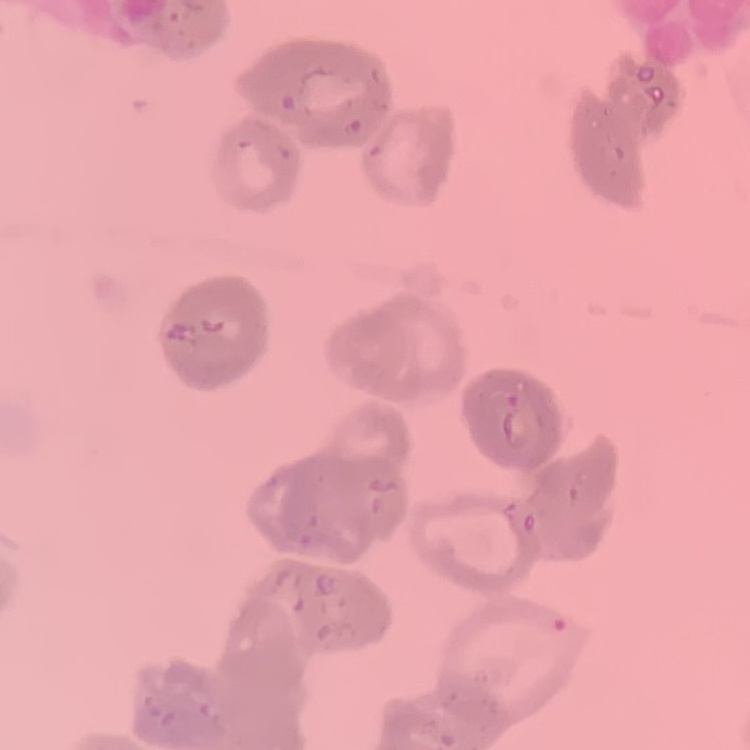 The erythrocytes show rouleaux formation. Field's or Giemsa stain. Thin blood film. One tile cut from a larger photomicrograph.